Identify the preparation type.
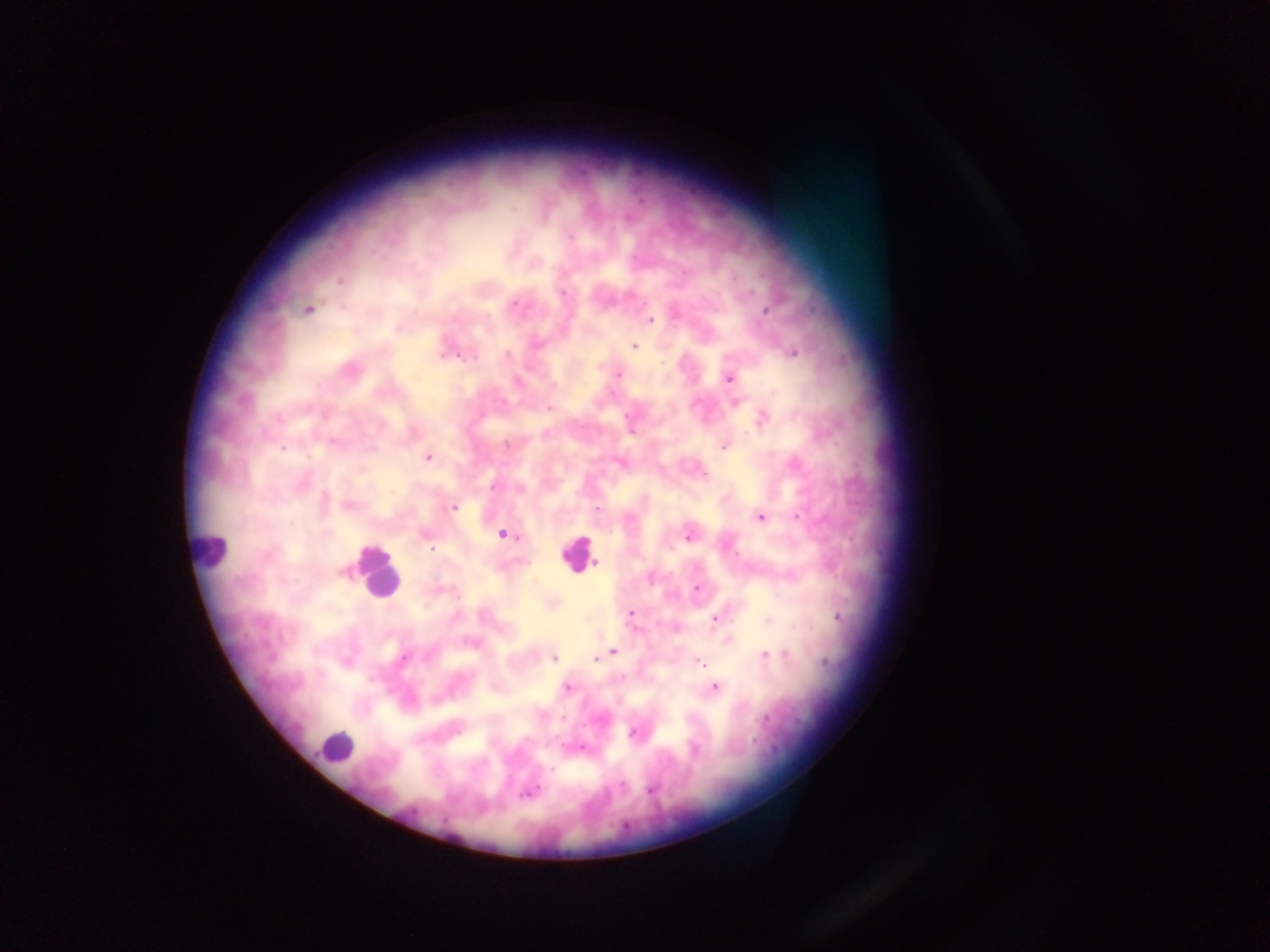

Thick blood smear.

Approximate centers as [x, y] in pixels. Plasmodium parasite locations: [569, 236], [562, 293], [630, 295], [515, 304], [307, 310], [767, 310], [650, 320], [536, 344], [634, 346], [793, 353], [507, 354], [443, 355], [459, 357], [475, 358], [618, 375], [729, 378], [517, 380], [549, 408], [629, 417], [763, 418], [506, 444], [724, 446], [282, 449], [427, 458], [703, 473], [303, 484], [493, 487], [349, 505], [453, 508], [598, 509], [760, 517], [799, 517], [503, 534], [425, 535], [688, 536], [430, 549], [596, 563], [344, 572], [698, 588], [631, 612], [838, 617], [715, 620], [613, 652], [765, 655], [554, 658], [404, 659], [596, 659], [826, 662], [701, 663], [567, 687], [715, 687], [633, 733], [583, 748], [552, 769], [622, 785], [650, 790], [529, 793]. Leukocyte locations: [211, 549], [578, 554], [377, 574], [335, 746]. Mobile-phone photograph taken through the microscope. Image is 1270×952 pixels. Collected in Ghana. Single field of view.